Classify this cell by malaria status.
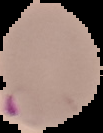
Parasitized.

Segmented cell region on a black background. From a thin blood film. Image is 103×133 pixels.